Give the position of every malaria parasite.
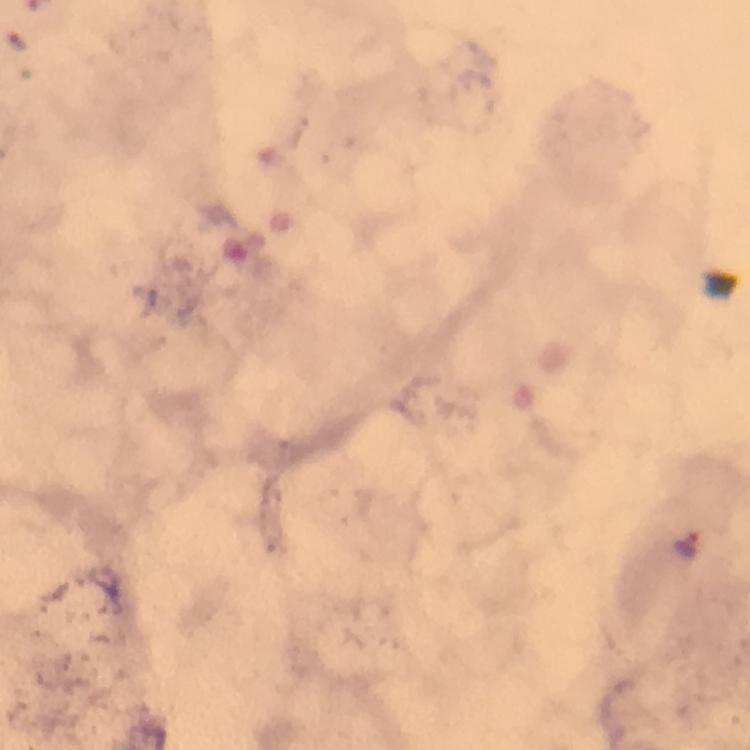
Approximate centers as (x, y) in pixels.
Malaria parasites: (690, 545).

stain: Giemsa
immersion_oil: applied
capture: smartphone camera through the microscope
image_size: 750×750 pixels
preparation: thick blood smear
cropped_from: a single field of view
context: from a diagnostic examination for malaria
magnification: 100x